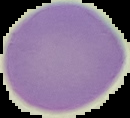 Image is 130×118 pixels. Malaria status: uninfected. From a thin blood smear. The area outside the segmented cell region is set to black.